Assess this cell for malaria.
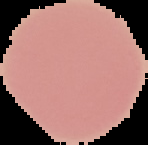

Uninfected.

From a thin blood smear. Segmented cell region on a black background. Image is 148×145 pixels.